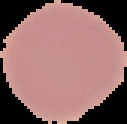
Summary:
  - Preparation: thin blood film
  - Image type: segmented cell region on a black background
  - Result: negative for malaria parasites
  - Image size: 127×124 pixels